Outline each Plasmodium falciparum-infected red blood cell.
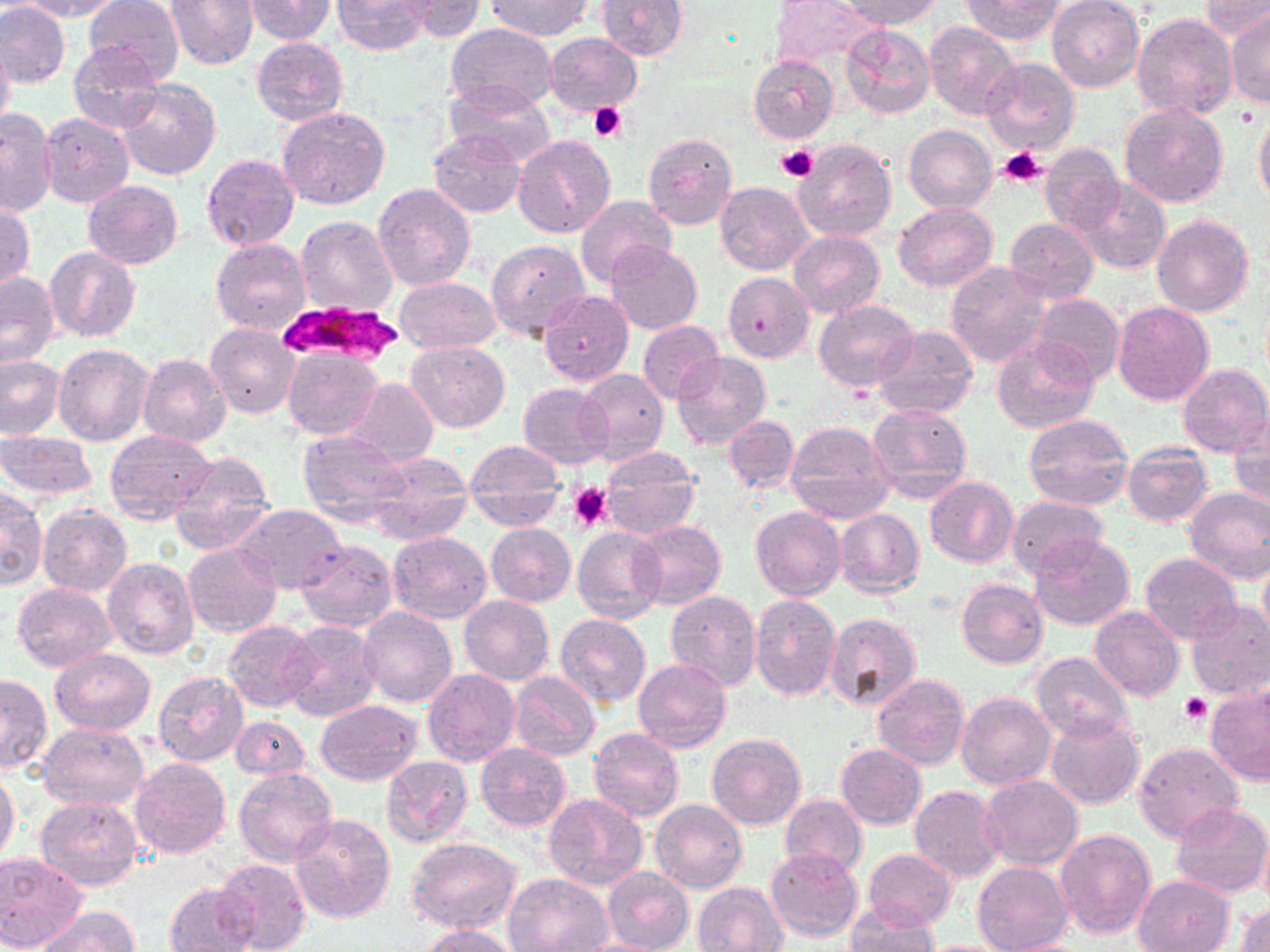

Approximate bounding boxes as (x1, y1, x2, y2) in pixels.
Plasmodium falciparum-infected red blood cells: (278, 303, 406, 367).

Summary:
  - Uninfected red blood cell locations: (0, 0, 70, 88), (21, 0, 124, 20), (83, 0, 184, 83), (166, 0, 260, 69), (244, 0, 337, 45), (331, 0, 430, 55), (398, 0, 486, 40), (487, 0, 591, 40), (597, 0, 688, 60), (769, 0, 877, 66), (839, 0, 943, 28), (964, 0, 1064, 44), (1047, 0, 1144, 92), (1199, 0, 1269, 41), (1225, 12, 1270, 108), (1131, 13, 1239, 121), (925, 22, 1021, 121), (446, 23, 556, 114), (841, 23, 935, 121), (543, 33, 642, 116), (252, 37, 348, 125), (0, 38, 13, 137), (69, 44, 166, 133), (748, 55, 838, 144), (979, 57, 1079, 154), (114, 78, 221, 181), (446, 83, 555, 168), (1118, 102, 1229, 208), (276, 106, 390, 209), (1, 109, 57, 219), (1255, 110, 1270, 208), (40, 113, 135, 210), (903, 126, 995, 213), (429, 130, 526, 216), (642, 132, 737, 231), (514, 134, 615, 238), (794, 139, 896, 242), (1039, 143, 1124, 233), (203, 153, 300, 251), (1071, 177, 1170, 274), (84, 181, 182, 269), (716, 181, 813, 276), (372, 183, 475, 291), (577, 196, 678, 288), (894, 201, 997, 292), (1, 202, 34, 292), (1152, 214, 1253, 317), (295, 215, 398, 317), (1003, 216, 1098, 303), (788, 231, 883, 318), (484, 238, 591, 341), (212, 239, 311, 335), (605, 242, 703, 336), (45, 248, 139, 342), (945, 264, 1048, 367), (722, 272, 814, 363), (0, 273, 60, 370), (394, 277, 500, 354), (538, 290, 633, 386), (1030, 293, 1124, 384), (814, 299, 919, 391), (1112, 301, 1214, 406), (637, 319, 724, 405), (205, 323, 301, 419), (872, 325, 977, 420), (992, 336, 1099, 433), (405, 339, 509, 431), (54, 343, 153, 445), (282, 347, 383, 439), (138, 353, 231, 449), (672, 353, 771, 449), (0, 355, 64, 439), (1179, 363, 1270, 457), (578, 369, 668, 462), (344, 377, 437, 465), (518, 383, 613, 468), (866, 403, 973, 504), (1230, 413, 1270, 513), (1022, 414, 1133, 511), (724, 416, 799, 492), (784, 421, 895, 523), (297, 429, 412, 525), (105, 430, 218, 523), (0, 431, 100, 500), (464, 439, 565, 530), (1121, 444, 1212, 527), (600, 448, 700, 541), (366, 451, 473, 546), (167, 452, 274, 556), (924, 476, 1018, 567), (1, 486, 47, 591), (1185, 487, 1270, 584), (1006, 495, 1108, 579), (38, 504, 131, 597), (235, 504, 347, 595), (751, 505, 845, 600), (835, 509, 924, 597), (631, 520, 725, 608), (485, 523, 576, 607), (573, 527, 666, 624), (387, 530, 492, 625), (1028, 535, 1134, 631), (296, 539, 397, 631), (184, 543, 281, 637), (1140, 552, 1242, 644), (1258, 555, 1270, 645), (103, 557, 198, 659), (956, 577, 1049, 668), (13, 582, 116, 673), (664, 590, 761, 691), (459, 594, 552, 685), (750, 594, 841, 700), (1185, 600, 1270, 700), (358, 606, 457, 708), (1090, 608, 1184, 702), (556, 613, 650, 707), (823, 613, 921, 712), (224, 621, 318, 711), (281, 621, 381, 723), (51, 648, 156, 736), (1030, 652, 1132, 743), (633, 658, 731, 751), (423, 669, 520, 767), (510, 670, 600, 759), (154, 672, 248, 767), (0, 673, 51, 776), (873, 674, 969, 771), (1205, 684, 1269, 786), (956, 691, 1056, 790), (315, 701, 422, 785), (231, 715, 308, 781), (1045, 716, 1143, 809), (37, 720, 149, 811), (589, 727, 684, 820), (707, 734, 806, 830), (476, 742, 572, 831), (836, 742, 927, 829), (1133, 743, 1243, 842), (381, 755, 473, 847), (130, 757, 230, 859), (234, 767, 337, 867), (0, 772, 20, 866), (979, 775, 1084, 869), (254, 778, 382, 901), (910, 785, 1004, 881), (545, 794, 648, 892), (779, 795, 867, 878), (35, 797, 143, 891), (651, 799, 747, 893), (1169, 804, 1270, 899), (291, 812, 395, 923), (1259, 825, 1270, 916), (1055, 827, 1156, 940), (405, 836, 521, 933), (765, 848, 863, 941), (863, 849, 956, 929), (0, 852, 88, 951), (214, 857, 311, 952), (973, 861, 1073, 952), (601, 867, 693, 952), (504, 872, 613, 952), (1133, 874, 1234, 952), (164, 881, 258, 952), (693, 881, 790, 951), (1235, 901, 1270, 952), (845, 903, 938, 952), (40, 906, 139, 952), (421, 925, 520, 952)
  - Platelet locations: (589, 102, 627, 143), (775, 145, 818, 182), (998, 146, 1047, 187), (570, 483, 612, 532), (1179, 693, 1210, 725)
  - Slide-level diagnosis: Plasmodium falciparum
  - Magnification: 1000x
  - Modality: light microscopy
  - Stain: May-Grünwald-Giemsa
  - Image size: 1270×952 pixels
  - Preparation: thin blood film
  - Field of view: one of a larger specimen